Outline each blood parasite and name the species.
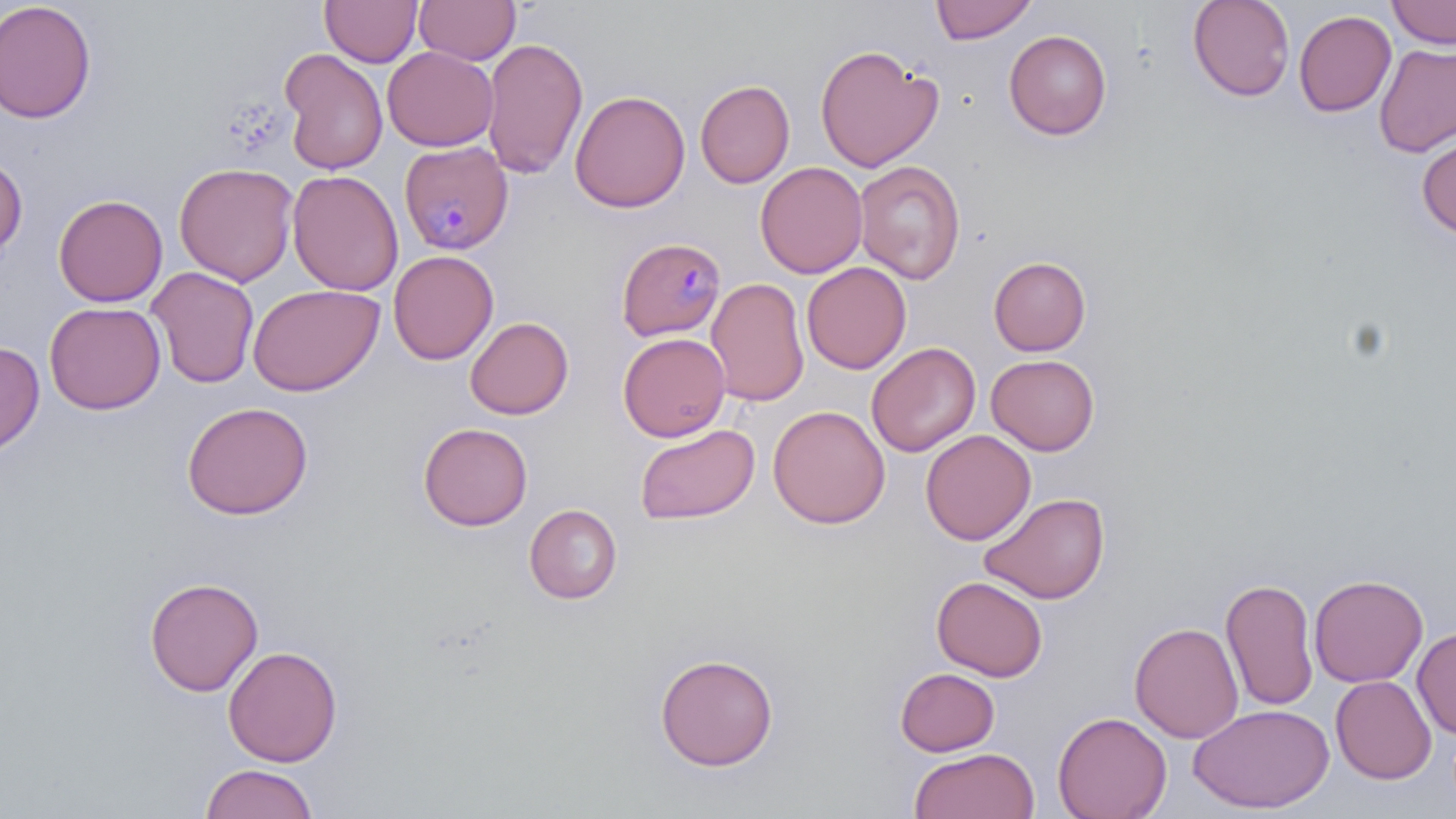
Approximate bounding boxes as (x1, y1, x2, y2) in pixels.
Plasmodium malariae-infected red blood cells: (394, 140, 515, 255), (616, 237, 726, 341).
No Plasmodium falciparum, Plasmodium ovale, Plasmodium vivax, Babesia divergens, or Trypanosoma brucei observed.

Summary:
  - Uninfected red blood cell locations: (320, 0, 422, 67), (414, 0, 521, 65), (930, 0, 1037, 44), (1187, 0, 1295, 102), (1387, 0, 1456, 49), (0, 1, 97, 123), (1293, 10, 1397, 117), (1004, 29, 1112, 140), (482, 36, 589, 180), (1374, 42, 1456, 157), (814, 43, 944, 172), (382, 46, 498, 151), (279, 48, 388, 175), (695, 79, 795, 188), (570, 89, 690, 213), (1417, 136, 1456, 238), (0, 153, 28, 260), (854, 160, 966, 284), (755, 161, 868, 279), (174, 162, 299, 287), (287, 170, 403, 296), (53, 194, 168, 307), (388, 250, 498, 365), (989, 256, 1091, 356), (801, 262, 911, 374), (145, 266, 260, 389), (706, 278, 809, 406), (247, 284, 383, 396), (45, 302, 166, 414), (465, 316, 573, 420), (617, 333, 730, 442), (0, 340, 45, 456), (867, 342, 980, 456), (986, 354, 1100, 455), (182, 401, 313, 520), (768, 405, 890, 528), (635, 418, 892, 528), (418, 422, 533, 531), (635, 423, 760, 525), (920, 429, 1036, 545), (979, 491, 1110, 604), (524, 503, 623, 604), (1309, 573, 1428, 687), (144, 575, 263, 697), (932, 575, 1047, 681), (1220, 576, 1319, 711), (1129, 621, 1244, 743), (1413, 628, 1456, 738), (223, 645, 342, 766), (654, 652, 779, 771), (895, 667, 1000, 756), (1331, 675, 1436, 783), (1189, 703, 1334, 814), (1053, 711, 1172, 819), (908, 747, 1039, 819), (200, 764, 319, 819)
  - Slide-level diagnosis: Plasmodium malariae
  - Field of view: one of a larger specimen
  - Stain: May-Grünwald-Giemsa
  - Magnification: 1000x
  - Modality: optical microscopy
  - Preparation: thin blood film
  - Image size: 1456×819 pixels